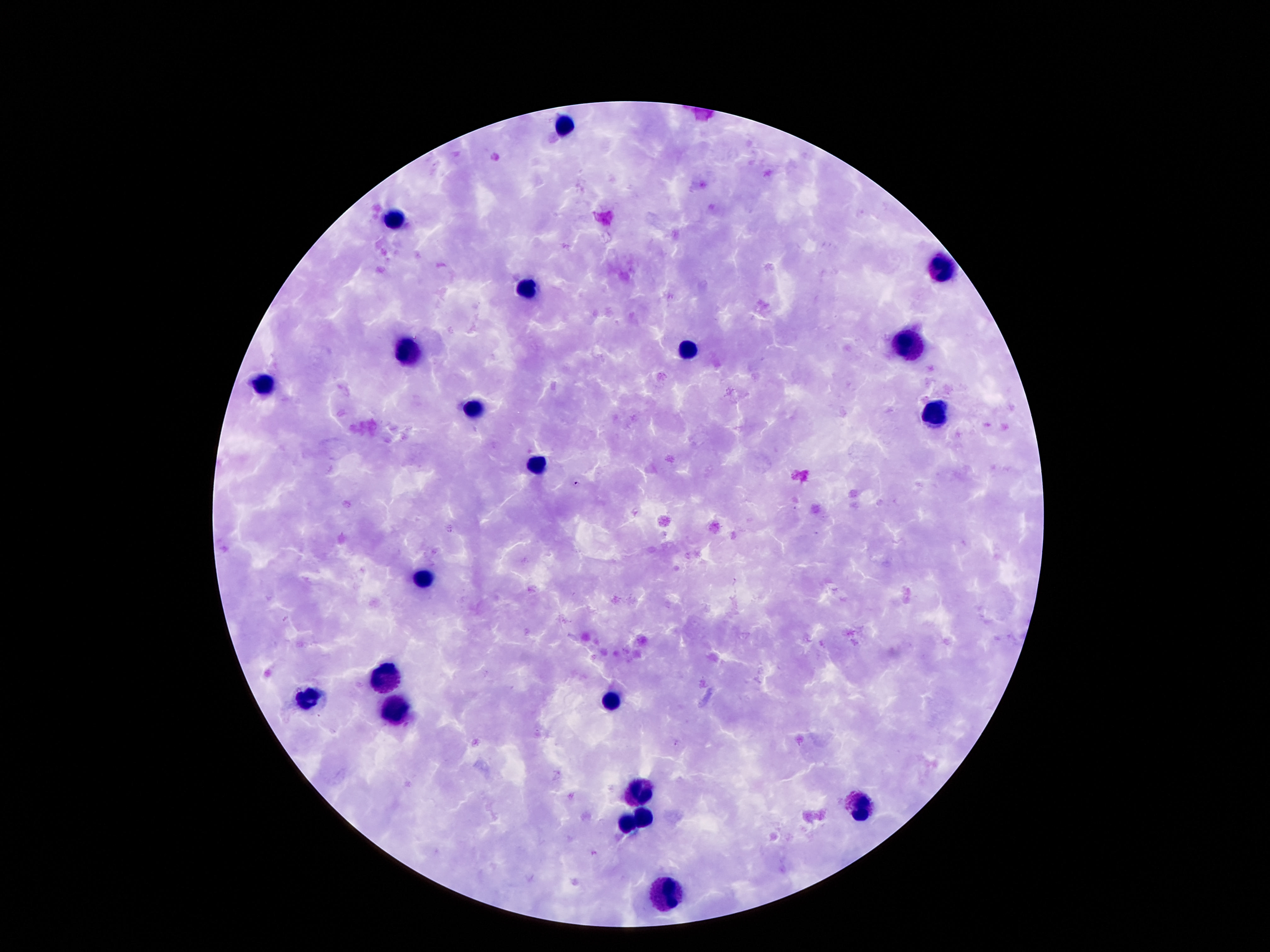

leukocyte locations = approximate centers as [x, y] in pixels: [563, 128], [393, 222], [945, 270], [526, 289], [904, 348], [685, 350], [406, 352], [263, 386], [473, 408], [934, 416], [533, 463], [418, 579], [384, 679], [307, 698], [612, 702], [393, 711], [639, 793], [857, 807], [639, 815], [627, 826], [667, 899]
field of view = one from this slide
capture = smartphone camera through the microscope eyepiece
preparation = thick blood smear
patient malaria status = uninfected
image size = 1270×952 pixels
stain = Giemsa
magnification = 100x